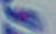
modality: photomicrograph
identification: Toxoplasma gondii
magnification: 1000x